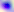 400x magnification. Photomicrograph. Toxoplasma gondii is shown.